Describe the morphology of the erythrocytes.
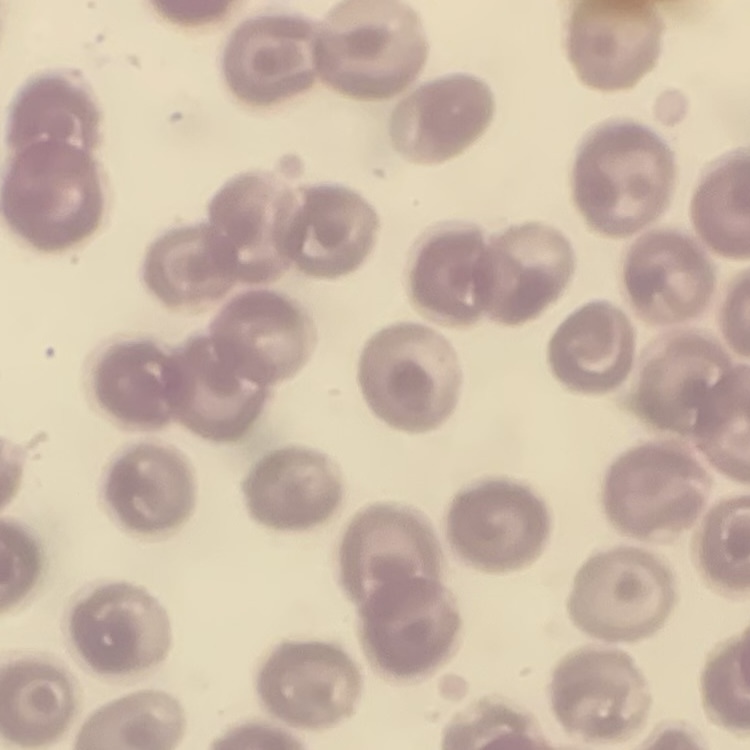

No rouleaux formation.

Square crop of a larger photomicrograph. Stained with either Field's or Giemsa. Thin peripheral smear.